Assess this cell for malaria.
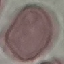
It is uninfected.

Summary:
  - Image type: automatically extracted cell patch, resized to 64 × 64 pixels
  - Preparation: thin blood film
  - Capture: smartphone camera at the microscope eyepiece
  - Stain: Giemsa